Assess this cell for malaria.
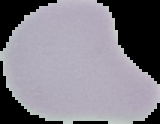
It is uninfected.

image type = segmented cell region on a black background
image size = 160×124 pixels
preparation = thin blood smear